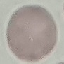
Summary:
  - Malaria status: uninfected
  - Preparation: thin blood smear
  - Stain: Giemsa
  - Capture: smartphone through the microscope eyepiece
  - Image type: cell patch, automatically extracted from a larger field of view and resized to 64 × 64 pixels